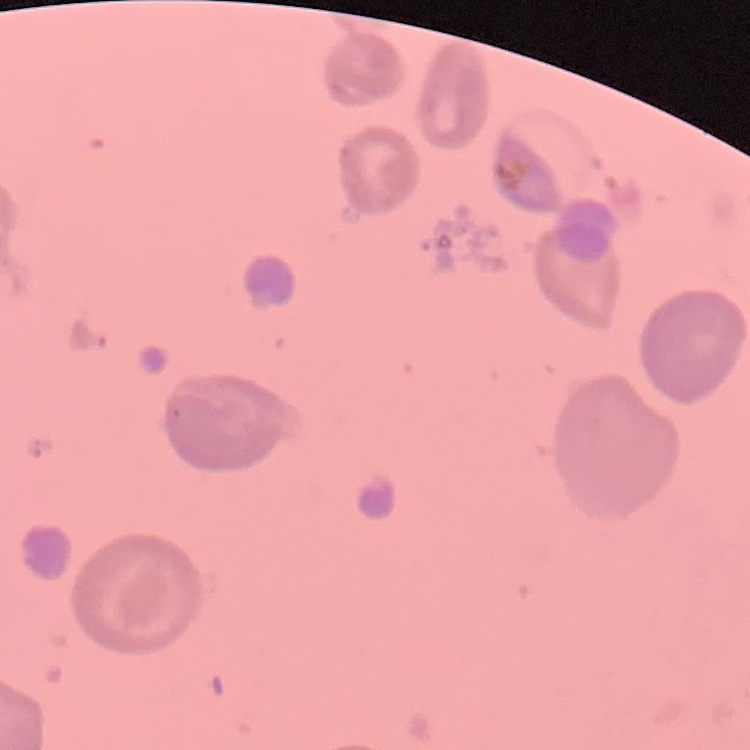
red blood cell morphology = no rouleaux formation
preparation = thin blood film
stain = Field's or Giemsa
image type = square crop of a larger photomicrograph